Classify this cell by malaria status.
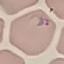
It is parasitized.

Summary:
  - Preparation: thin blood film
  - Image type: automatically extracted cell patch, resized to 64 × 64 pixels
  - Capture: smartphone through the microscope eyepiece
  - Stain: Giemsa